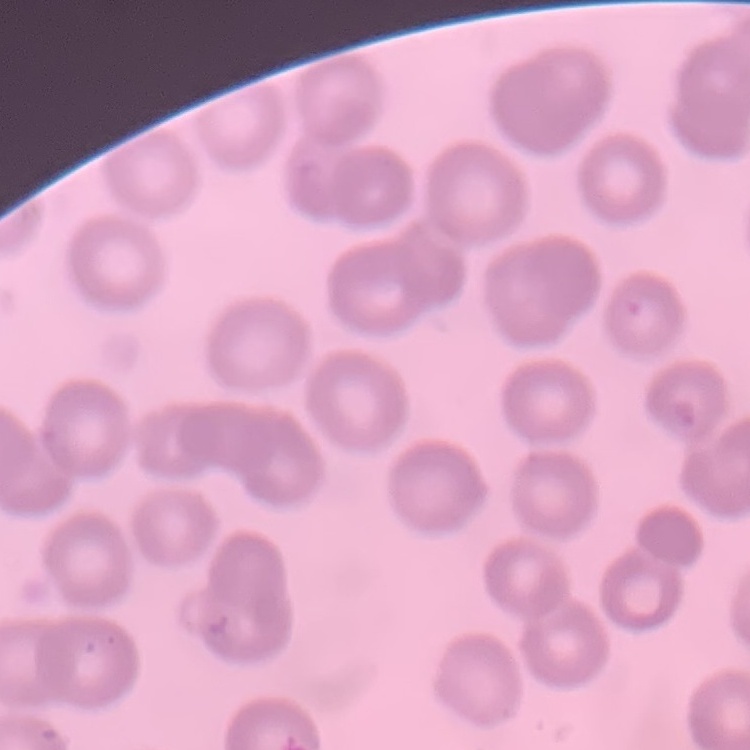
The red blood cells exhibit no rouleaux formation. Thin peripheral smear. One tile cut from a larger photomicrograph. Stained with either Field's or Giemsa.